Identify the preparation type.
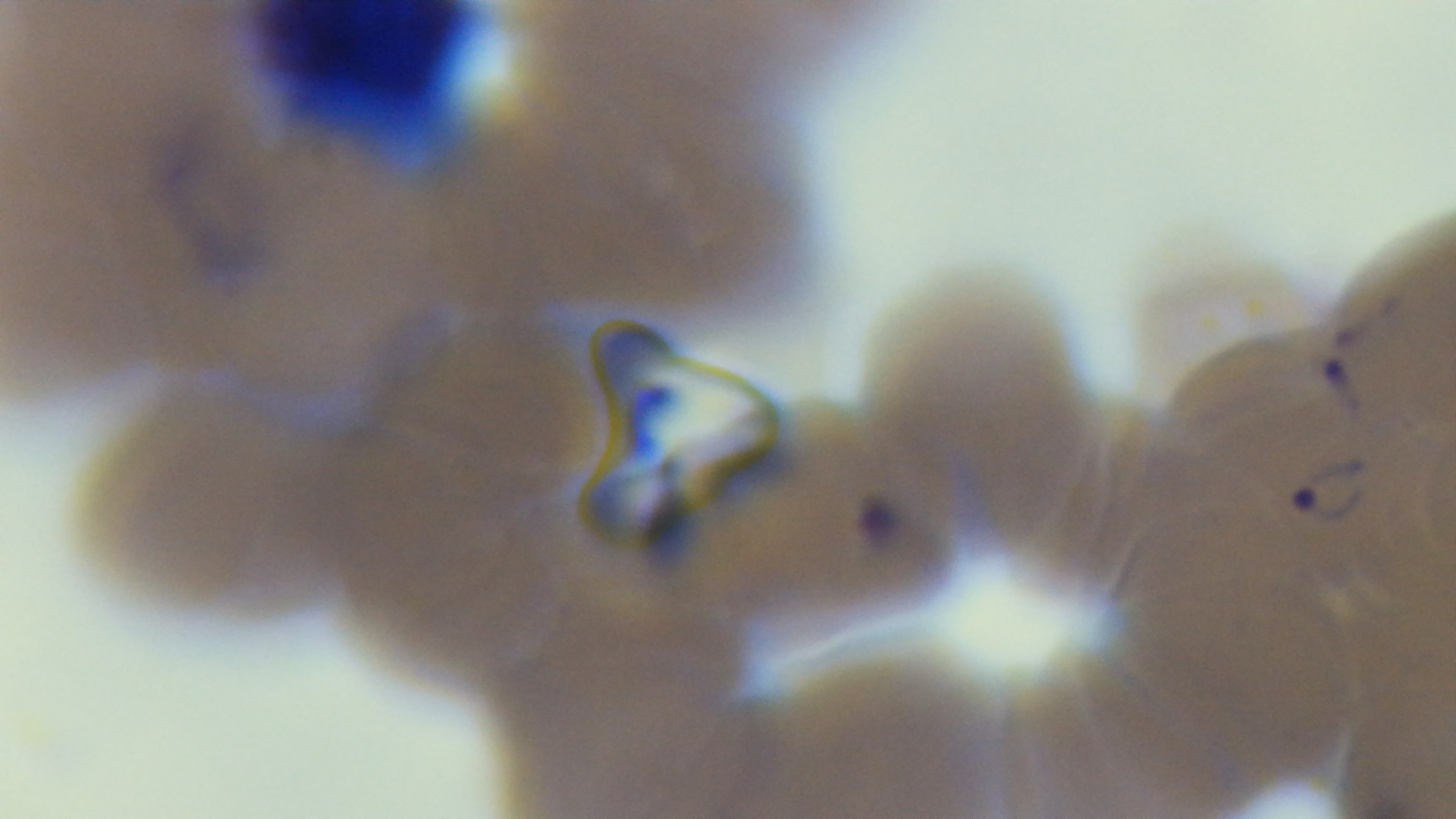
It is a thin blood film.

Summary:
  - Stain: Giemsa
  - Objective: 100x oil immersion
  - Field of view: one from the slide
  - Modality: light microscopy
  - Malaria status: positive
  - Capture: mounted 4K digital camera